Describe the morphology of the erythrocytes.
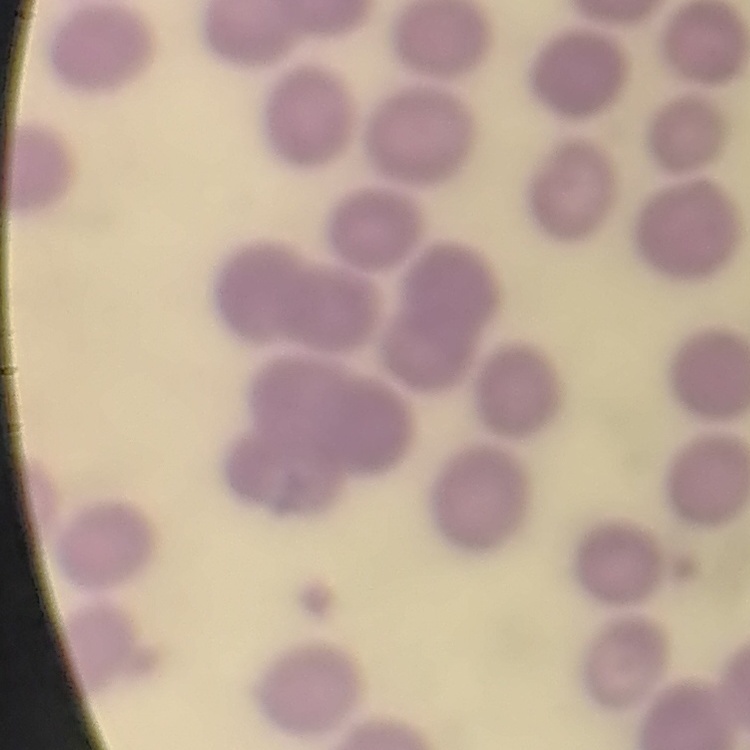

No rouleaux formation.

stain = Field's or Giemsa
image type = one tile cut from a larger photomicrograph
preparation = thin blood smear